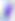
identification = Toxoplasma gondii
magnification = 400x
modality = micrograph